Name the cell type shown.
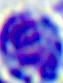

A leukocyte.

Summary:
  - Modality: micrograph
  - Magnification: 400x